Name the cell type shown.
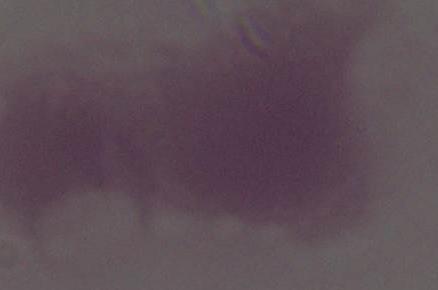

An erythrocyte.

Micrograph. 1000x magnification.